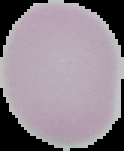 From a thin blood film. Image is 124×151 pixels. Segmented cell region on a black background. Malaria status: uninfected.